Identify the parasite.
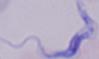
A trypanosome.

{
  "magnification": "1000x",
  "modality": "micrograph"
}